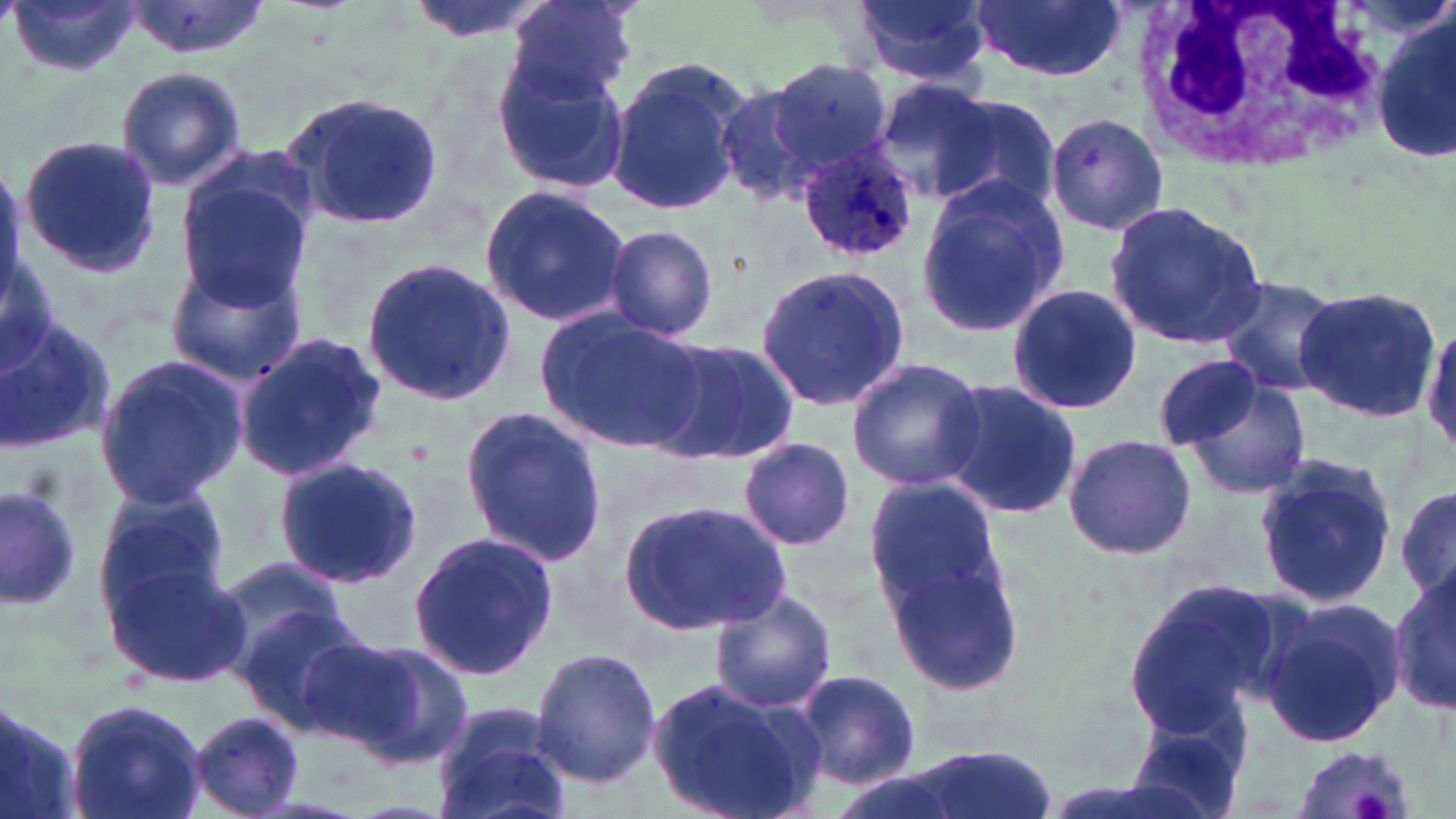

Approximate bounding boxes as (x1,y1)-(x2,y2) corner pairs in pixels. Platelet locations: (1350,786)-(1391,817). Uninfected red blood cell locations: (506,0)-(639,101), (851,0)-(993,86), (971,0)-(1127,82), (9,1)-(142,79), (120,1)-(269,59), (1374,14)-(1456,167), (490,52)-(629,194), (607,55)-(755,216), (766,59)-(893,178), (114,64)-(247,192), (872,79)-(997,204), (718,82)-(827,205), (283,89)-(444,231), (932,94)-(1061,214), (1040,109)-(1169,237), (18,136)-(160,273), (174,167)-(318,311), (914,173)-(1069,340), (477,184)-(633,327), (1104,201)-(1270,350), (603,224)-(719,343), (165,254)-(306,387), (359,258)-(520,406), (754,263)-(915,413), (1213,275)-(1342,397), (1005,283)-(1141,415), (1293,285)-(1441,423), (539,310)-(709,454), (0,315)-(116,453), (234,332)-(385,483), (644,336)-(799,467), (1153,351)-(1268,456), (93,354)-(249,511), (846,357)-(987,491), (1174,373)-(1312,501), (935,377)-(1084,521), (460,402)-(610,569), (1063,432)-(1198,562), (735,436)-(855,549), (274,457)-(421,587), (1253,457)-(1395,611), (864,476)-(1004,612), (0,483)-(86,611), (1394,484)-(1456,607), (91,485)-(228,615), (623,498)-(789,639), (408,531)-(556,683), (885,552)-(1026,694), (102,555)-(247,687), (213,555)-(349,670), (1388,562)-(1455,717), (1122,575)-(1289,741), (708,590)-(837,716), (1261,603)-(1404,750), (232,604)-(377,733), (276,625)-(420,749), (325,639)-(475,768), (532,646)-(660,787), (794,668)-(921,789), (648,676)-(823,819), (0,695)-(84,819), (64,698)-(208,819), (431,702)-(573,819), (1124,708)-(1255,819), (186,710)-(306,817), (1287,741)-(1416,819), (901,746)-(1057,819). White blood cell locations: (1127,0)-(1393,176). Plasmodium ovale-infected red blood cell locations: (796,142)-(919,263). Slide-level diagnosis: Plasmodium ovale. 1000x magnification. One field of a larger specimen. Thin blood film. May-Grünwald-Giemsa stain. Light microscopy. Image is 1456×819 pixels.